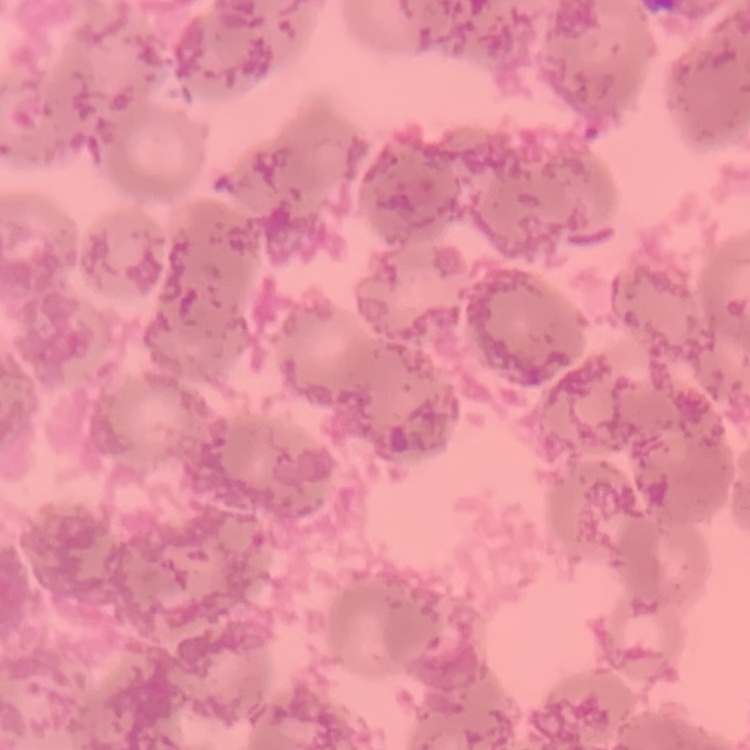

{
  "erythrocyte_morphology": "rouleaux formation",
  "stain": "Field's or Giemsa",
  "preparation": "thin peripheral smear",
  "image_type": "one tile cut from a larger photomicrograph"
}